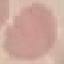
Summary:
  - Malaria status: uninfected
  - Capture: smartphone through the microscope eyepiece
  - Image type: automatically extracted cell patch, resized to 64 × 64 pixels
  - Stain: Giemsa
  - Preparation: thin smear